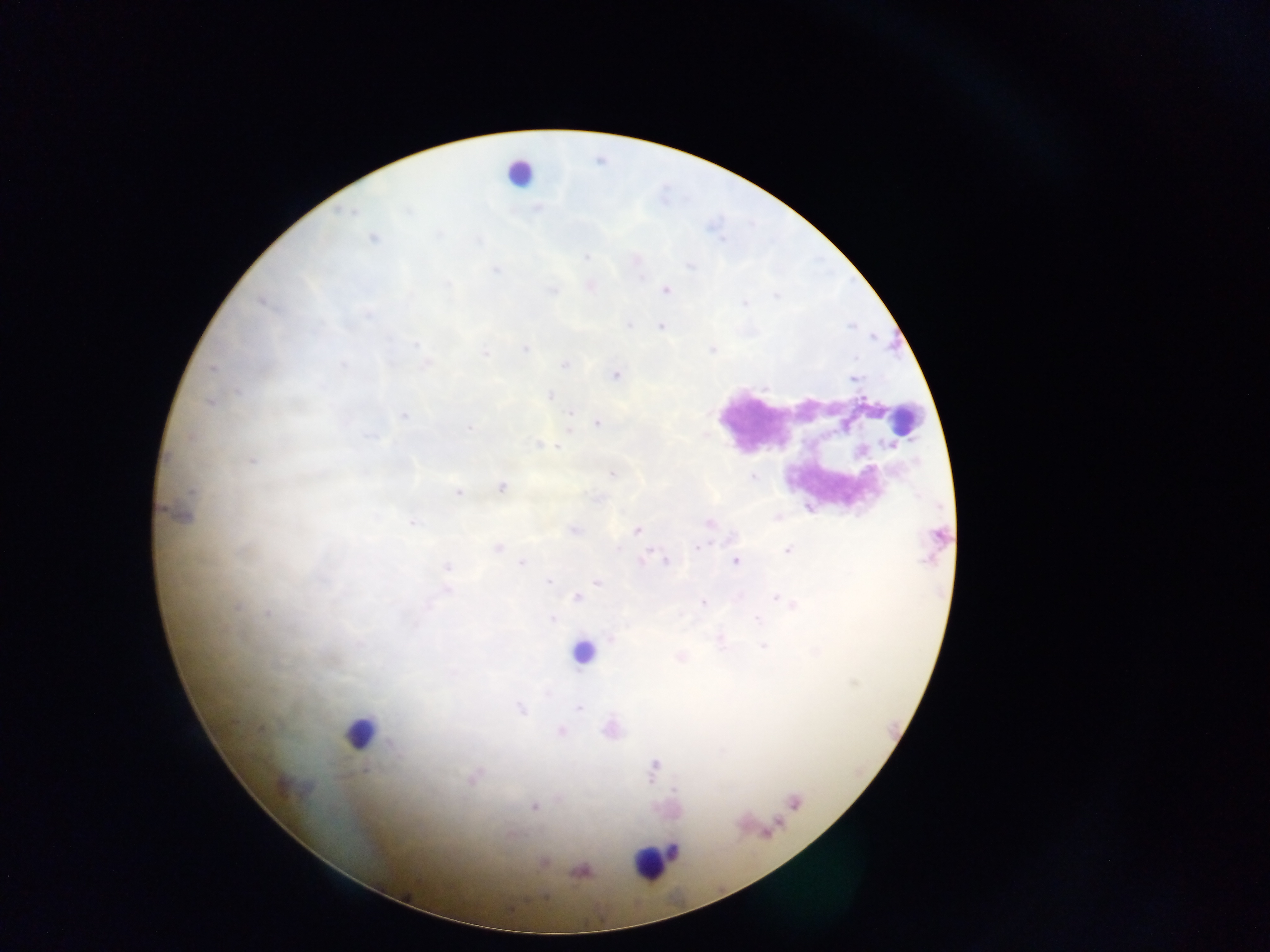
Approximate centers as x y in pixels. Malaria parasite locations: 373 238; 591 286; 665 289; 661 327; 526 348; 565 363; 614 375; 853 378; 550 396; 210 402; 404 416; 597 422; 561 447; 251 460; 612 473; 502 487; 458 492; 178 513; 777 518; 412 521; 573 530; 636 531; 497 548; 788 550; 652 552; 734 560; 522 562; 448 567; 549 582; 598 582; 577 598; 702 602; 266 613; 551 617; 764 646; 680 656; 519 708; 559 731; 472 779; 534 806; 541 862; 580 870. Leukocyte locations: 519 173; 902 421; 583 651; 360 733; 793 802; 653 860. Sample from Ghana. Image is 1270×952 pixels. Mobile-phone photograph taken through the microscope. Thick blood smear. One field of view.